Locate every blood parasite and identify its species.
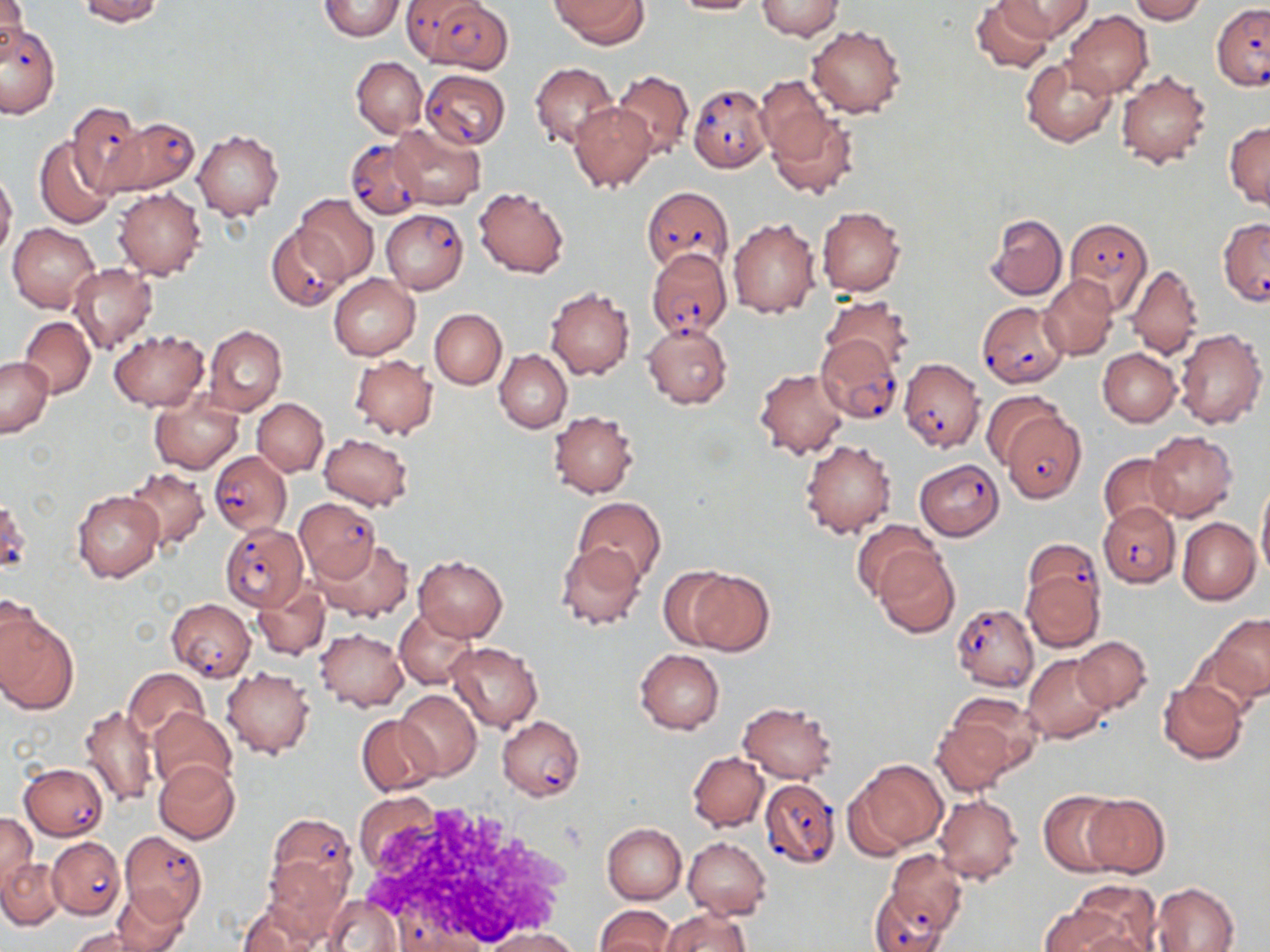

Approximate bounding boxes as (x1, y1, x2, y2) in pixels.
Plasmodium falciparum-infected red blood cells: (422, 0, 513, 72), (1211, 3, 1270, 92), (0, 22, 60, 118), (421, 70, 510, 148), (688, 85, 771, 172), (66, 103, 149, 195), (102, 116, 200, 197), (345, 137, 428, 219), (641, 185, 733, 272), (381, 210, 467, 294), (1066, 215, 1152, 311), (1216, 217, 1270, 304), (266, 225, 348, 311), (645, 247, 733, 340), (976, 300, 1069, 388), (816, 335, 903, 425), (898, 358, 984, 452), (998, 410, 1087, 502), (209, 450, 291, 536), (914, 458, 1006, 540), (0, 499, 32, 579), (295, 499, 379, 580), (1098, 501, 1180, 588), (219, 523, 307, 610), (1023, 538, 1104, 621), (167, 598, 255, 679), (951, 604, 1040, 691), (497, 716, 584, 801), (20, 763, 108, 840), (761, 779, 839, 867), (265, 813, 357, 910), (119, 831, 206, 922), (47, 837, 124, 919), (882, 849, 967, 937), (869, 889, 950, 952), (398, 912, 481, 952).
No Plasmodium ovale, Plasmodium malariae, Plasmodium vivax, Babesia divergens, or Trypanosoma brucei observed.

Summary:
  - Uninfected red blood cell locations: (0, 0, 27, 59), (78, 0, 164, 25), (317, 0, 406, 41), (552, 0, 648, 48), (671, 0, 762, 16), (970, 0, 1052, 74), (1001, 0, 1091, 41), (1129, 0, 1205, 24), (756, 1, 843, 40), (1064, 10, 1152, 98), (806, 25, 905, 117), (1021, 55, 1117, 147), (351, 56, 428, 137), (530, 62, 618, 151), (612, 70, 693, 158), (1115, 71, 1212, 169), (757, 75, 836, 168), (569, 103, 656, 190), (768, 111, 858, 200), (1225, 120, 1270, 211), (389, 122, 485, 209), (192, 129, 284, 220), (35, 137, 118, 229), (0, 170, 17, 260), (473, 187, 568, 278), (115, 188, 206, 279), (295, 194, 377, 283), (817, 205, 906, 297), (986, 214, 1067, 300), (727, 216, 820, 317), (6, 223, 98, 311), (70, 263, 157, 356), (1125, 264, 1204, 360), (329, 275, 420, 360), (1040, 275, 1118, 359), (545, 285, 635, 379), (820, 294, 913, 376), (430, 308, 507, 388), (19, 316, 95, 398), (642, 322, 732, 409), (205, 326, 286, 415), (109, 329, 208, 411), (1174, 329, 1267, 429), (1098, 348, 1181, 427), (495, 350, 572, 432), (350, 354, 437, 439), (0, 357, 53, 438), (755, 369, 851, 458), (150, 390, 243, 474), (982, 390, 1067, 470), (252, 398, 328, 475), (549, 410, 641, 499), (1144, 429, 1238, 521), (319, 434, 415, 511), (800, 438, 897, 539), (1100, 453, 1180, 529), (124, 467, 209, 551), (1256, 479, 1270, 579), (73, 490, 163, 582), (574, 497, 665, 583), (1178, 517, 1260, 604), (852, 520, 942, 603), (314, 536, 412, 623), (556, 542, 645, 630), (873, 550, 960, 638), (413, 556, 508, 642), (657, 567, 739, 649), (685, 569, 775, 656), (1021, 569, 1104, 652), (252, 582, 331, 659), (0, 607, 78, 716), (393, 608, 474, 689), (1206, 613, 1270, 705), (314, 627, 407, 711), (1070, 636, 1151, 714), (446, 642, 543, 732), (635, 650, 724, 734), (1023, 653, 1114, 745), (221, 666, 315, 759), (123, 668, 208, 743), (1157, 678, 1248, 765), (396, 689, 482, 778), (943, 690, 1042, 779), (738, 701, 837, 783), (78, 705, 159, 808), (148, 708, 236, 791), (357, 715, 443, 797), (929, 715, 1020, 796), (688, 752, 768, 832), (846, 758, 948, 856), (153, 759, 241, 844), (355, 790, 443, 875), (1039, 790, 1123, 876), (933, 794, 1024, 885), (1082, 794, 1170, 878), (0, 813, 38, 894), (602, 822, 687, 904), (682, 837, 771, 920), (264, 852, 352, 939), (1, 858, 64, 928), (1067, 880, 1162, 952), (1152, 881, 1239, 952), (110, 887, 193, 949), (326, 894, 402, 952), (238, 900, 325, 952), (595, 904, 675, 952), (1038, 905, 1135, 952), (661, 909, 751, 952), (479, 927, 583, 951), (69, 928, 159, 952)
  - Slide-level diagnosis: Plasmodium falciparum
  - Preparation: thin blood film
  - Magnification: 1000x
  - Image size: 1270×952 pixels
  - Modality: optical microscopy
  - Stain: May-Grünwald-Giemsa
  - Field of view: single